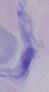

Captured at 1000x magnification. A trypanosome is shown. Micrograph.